Name the cell type shown.
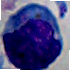
This is a leukocyte.

magnification: 1000x
modality: photomicrograph